Give the position of every leukocyte visible.
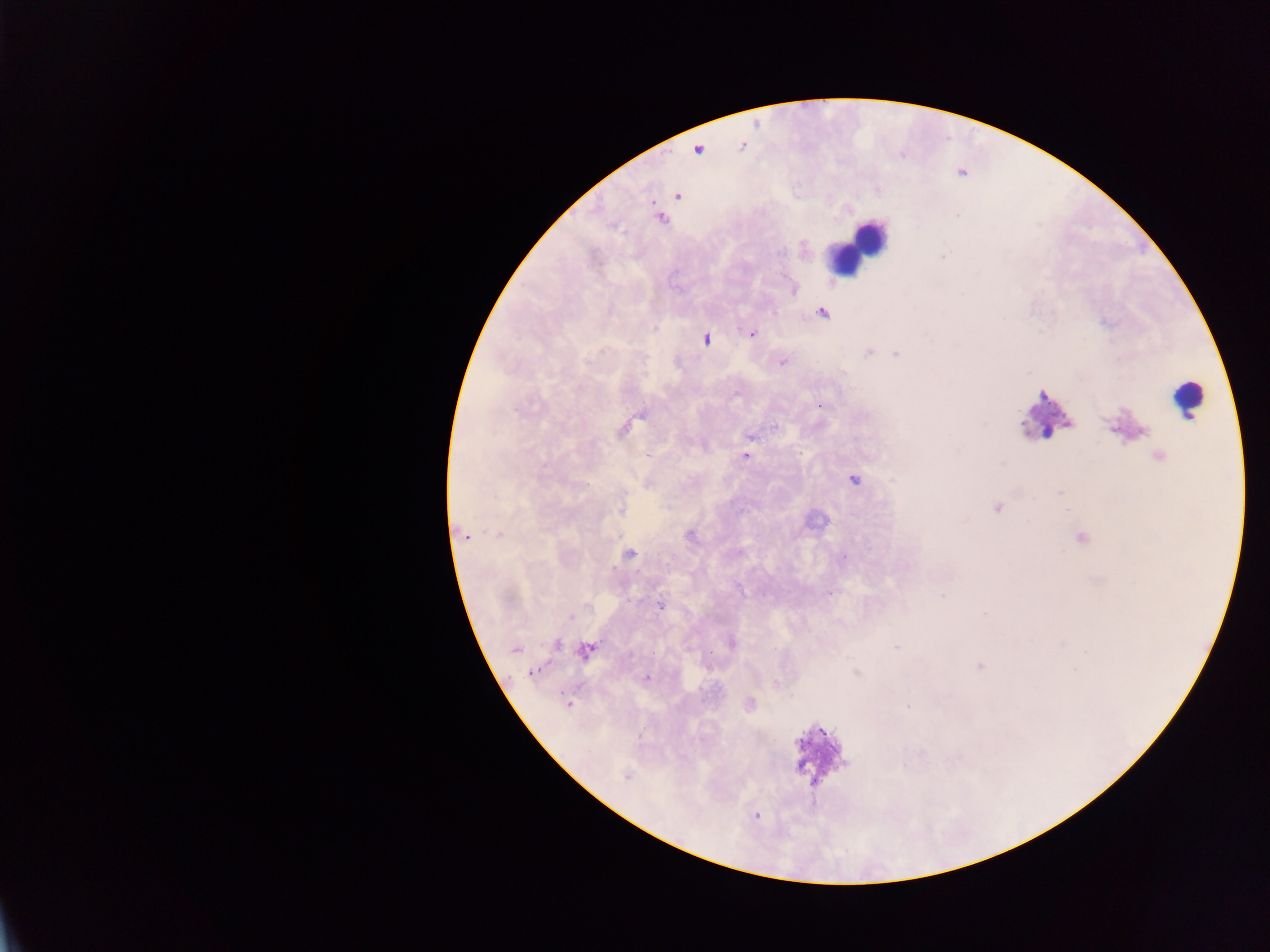

Approximate centers as (x, y) in pixels.
Leukocytes: (859, 243), (845, 260), (1187, 397), (1042, 410).

Summary:
  - Plasmodium parasite locations: (678, 196), (661, 219), (943, 256), (822, 313), (751, 333), (705, 339), (869, 352), (896, 353), (783, 362), (822, 405), (775, 426), (623, 428), (751, 436), (646, 454), (745, 456), (1159, 456), (854, 480), (1060, 492), (996, 508), (621, 509), (498, 534), (690, 535), (465, 537), (1082, 538), (629, 553), (843, 557), (943, 595), (660, 605), (571, 618), (731, 643), (557, 644), (896, 647), (515, 649), (585, 651), (979, 666), (533, 672), (646, 678), (775, 683), (568, 704), (750, 704), (907, 707), (626, 777), (756, 817)
  - Field of view: single
  - Image size: 1270×952 pixels
  - Country: Ghana
  - Preparation: thick blood smear
  - Capture: mobile-phone photograph through a microscope